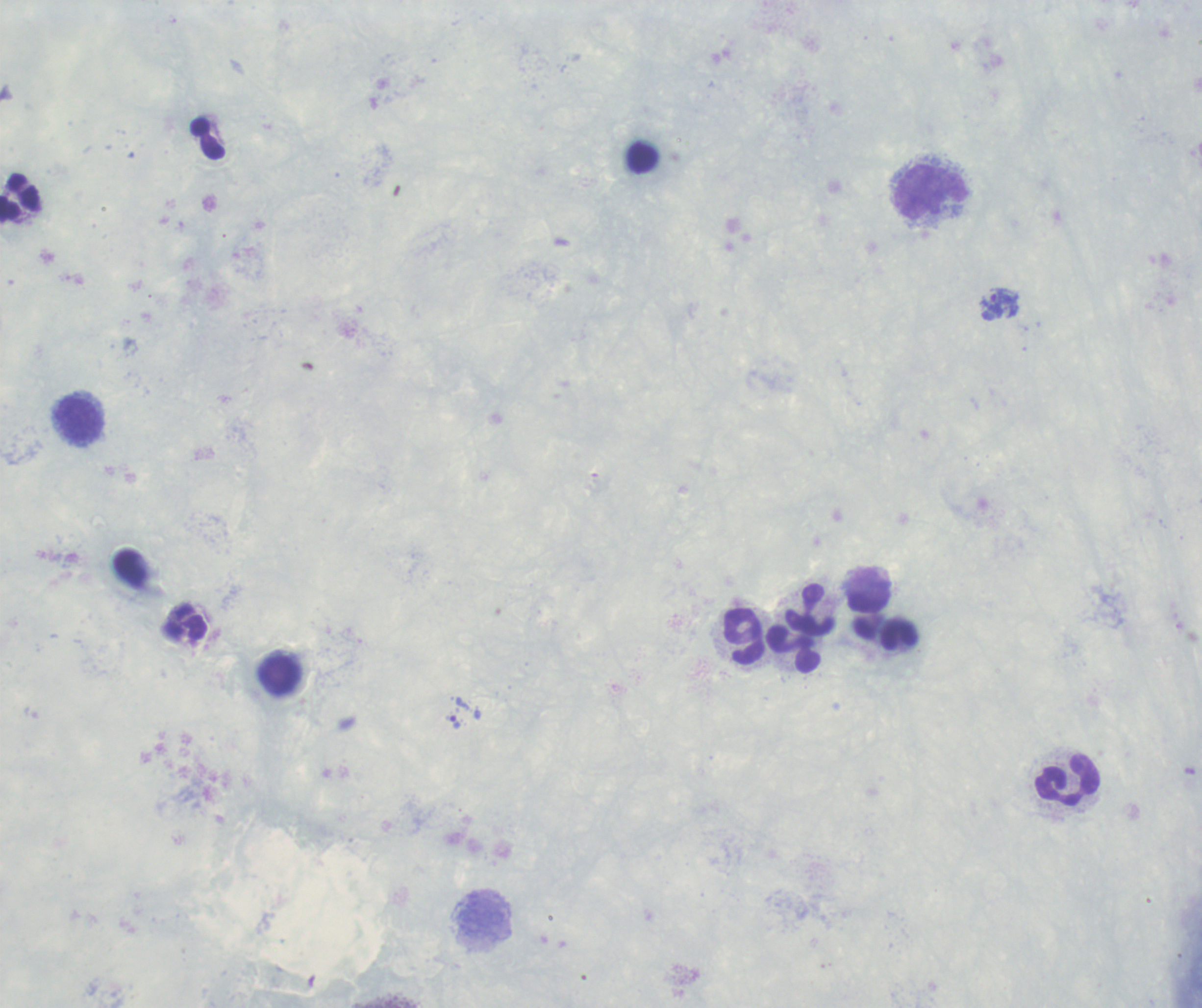
{
  "context": "previously used in a real diagnosis",
  "result": "malaria parasites identified",
  "coloration_quality": "good",
  "background_quality": "poor",
  "magnification": "100x",
  "trophozoite_locations": "approximate centers as {x, y} in pixels: {1000, 303}, {455, 722}",
  "stain": "Romanowsky",
  "leukocyte_locations": "approximate centers as {x, y} in pixels: {930, 191}, {19, 199}, {78, 420}, {868, 602}, {809, 609}, {186, 624}, {898, 634}, {743, 636}, {794, 649}, {280, 675}, {1067, 780}, {484, 915}",
  "preparation": "thick blood film",
  "image_size": "1202×1008 pixels",
  "field_of_view": "one from this slide"
}